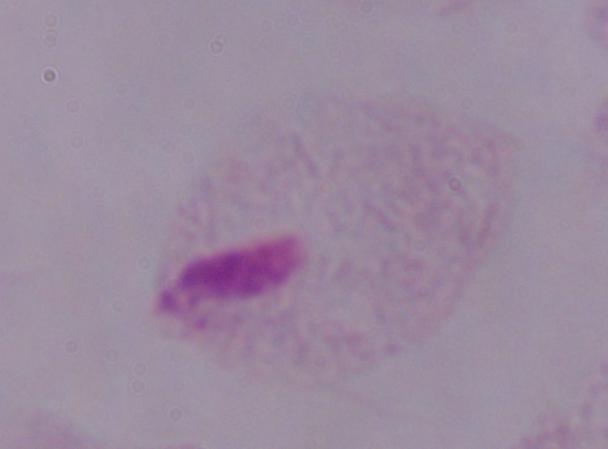

Summary:
  - Magnification: 1000x
  - Modality: micrograph
  - Identification: trichomonad